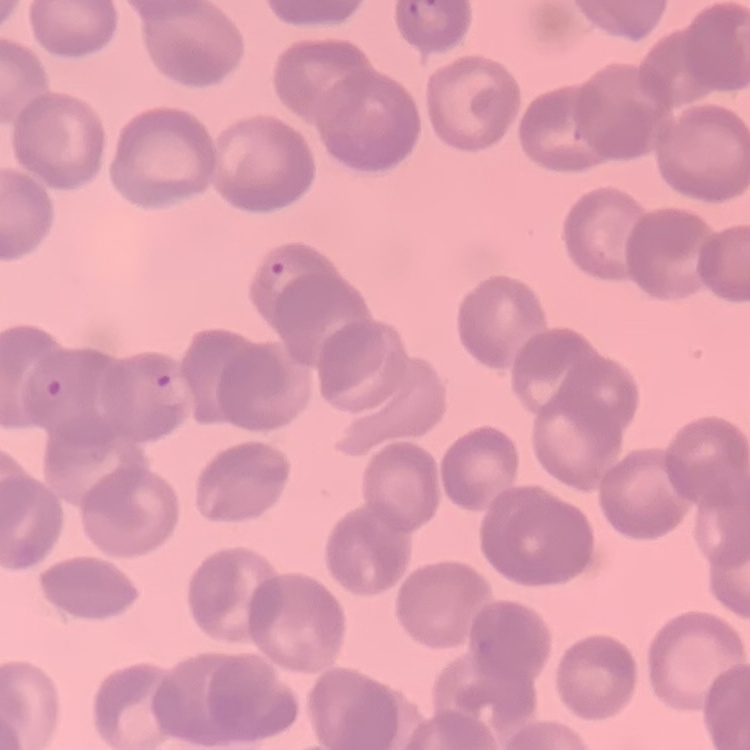

Summary:
  - Erythrocyte morphology: rouleaux formation
  - Image type: one tile cut from a larger photomicrograph
  - Preparation: thin blood smear
  - Stain: Field's or Giemsa